Assess this cell for malaria.
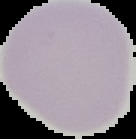

Uninfected.

image type = segmented cell region with the area outside set to black
preparation = thin blood smear
image size = 136×139 pixels